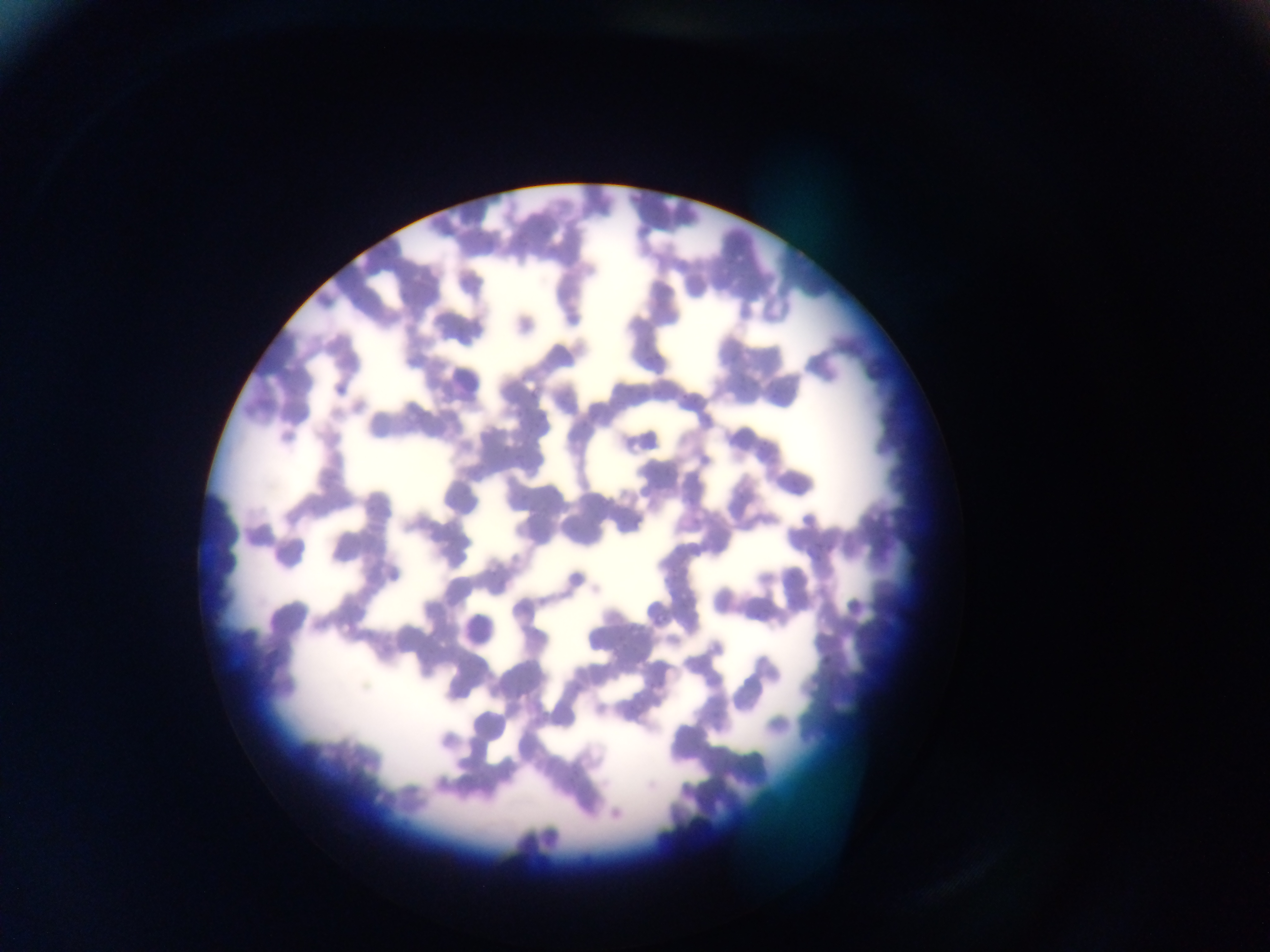

capture = mobile-phone photograph through a microscope
image size = 1270×952 pixels
country = Ghana
leukocyte locations = approximate bounding boxes as {left, top, right, bottom} in pixels: {440, 355, 484, 400}
field of view = single
preparation = thin blood smear